Locate malaria parasites and leukocytes.
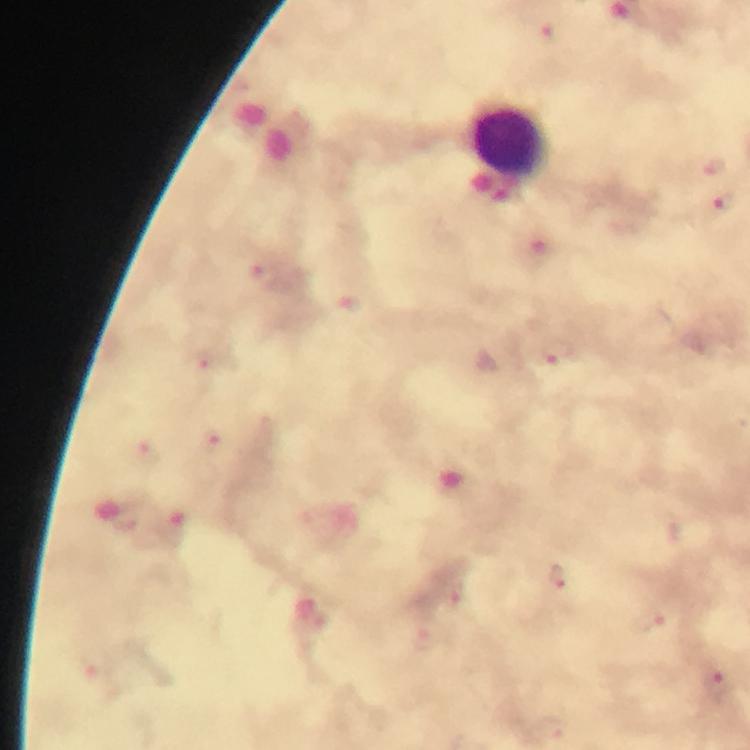

Approximate object centers, in pixels from the top-left corner.
Malaria parasites: (x=550, y=36), (x=715, y=168), (x=725, y=203), (x=266, y=276), (x=558, y=354), (x=203, y=361), (x=213, y=442), (x=150, y=456), (x=559, y=578), (x=656, y=621), (x=716, y=680).
Leukocytes: (x=511, y=141).

Summary:
  - Image size: 750×750 pixels
  - Immersion oil: used
  - Cropped from: a single field of view
  - Stain: Giemsa
  - Magnification: 100x
  - Context: from a diagnostic examination for malaria
  - Preparation: thick blood smear
  - Capture: smartphone photograph through a microscope